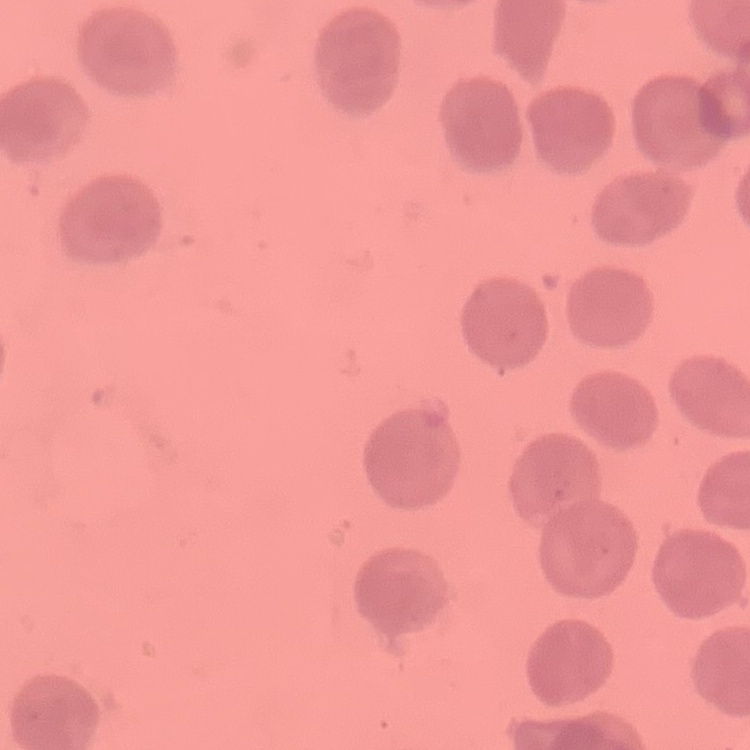
Summary:
  - Erythrocyte morphology: no rouleaux formation
  - Preparation: thin peripheral smear
  - Image type: one tile cut from a larger photomicrograph
  - Stain: Field's or Giemsa